Assess this cell for malaria.
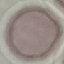
It is uninfected.

capture: smartphone camera at the microscope eyepiece
image_type: cell patch, automatically extracted from a larger field of view and resized to 64 × 64 pixels
stain: Giemsa
preparation: thin blood smear